Classify this cell by malaria status.
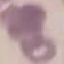

It is uninfected.

Giemsa stain. Acquired by smartphone through the microscope eyepiece. Thin blood film. Cell patch, automatically extracted from a larger field of view and resized to 64 × 64 pixels.